State the preparation type.
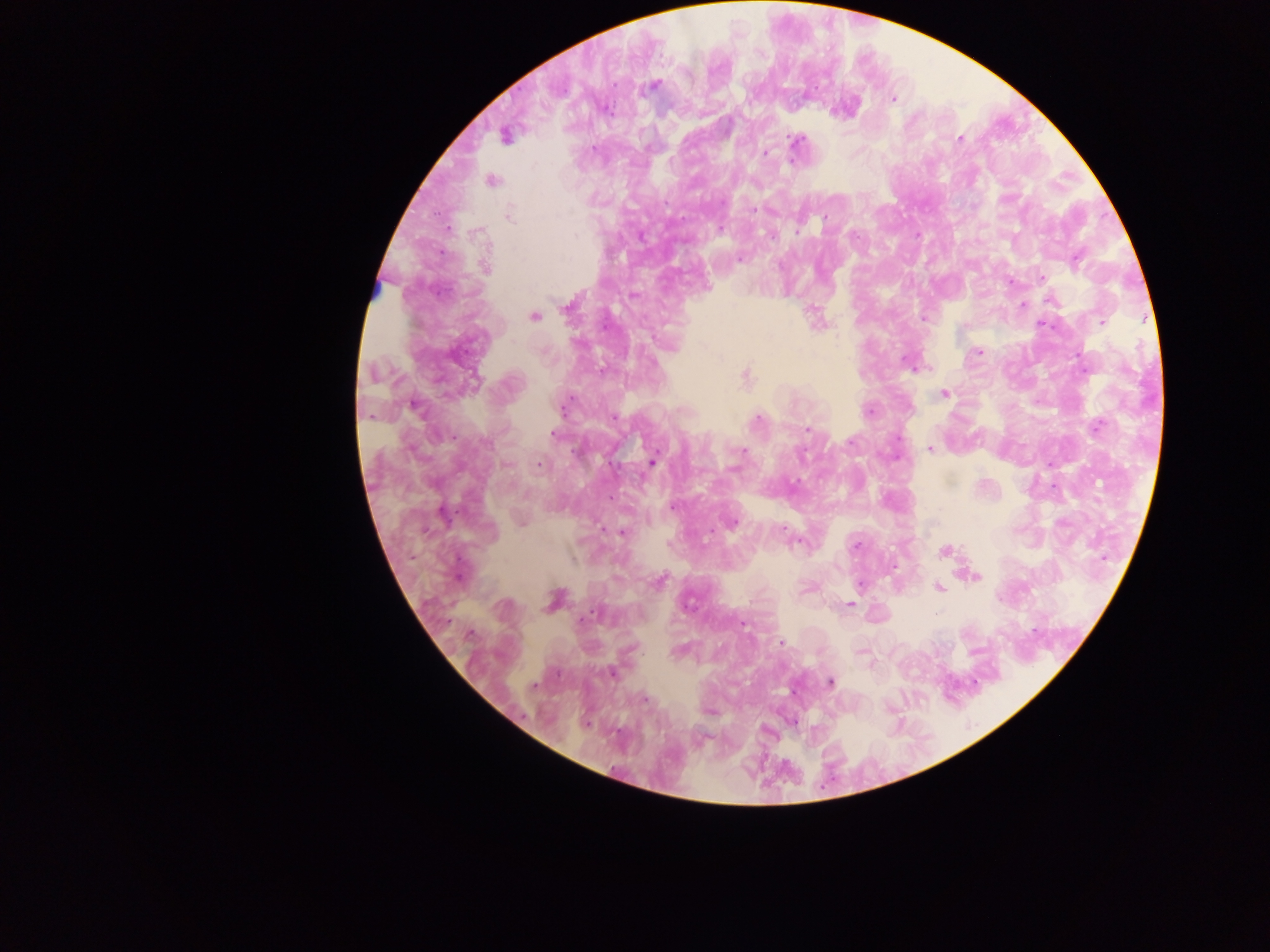

This is a thick smear.

Approximate centers as x y in pixels.
Summary:
  - Malaria parasite locations: 654 86; 893 99; 505 136; 959 139; 796 140; 593 150; 765 153; 492 181; 754 209; 509 216; 719 229; 797 231; 741 259; 486 267; 1042 278; 633 295; 1051 300; 1022 305; 534 317; 923 318; 1101 322; 816 323; 1042 325; 979 351; 905 360; 745 377; 944 394; 564 407; 415 408; 869 412; 369 416; 614 417; 757 419; 1098 426; 808 429; 553 434; 851 441; 486 443; 929 449; 742 452; 653 461; 539 465; 734 468; 672 508; 733 522; 521 523; 783 530; 621 533; 799 543; 855 546; 945 550; 974 576; 659 582; 859 585; 939 587; 554 600; 849 604; 588 616; 470 633; 780 643; 862 652; 612 673; 830 682; 534 686; 645 699
  - Field of view: single
  - Capture: mobile-phone photograph through a microscope
  - Country: Ghana
  - Image size: 1270×952 pixels